Assess for Plasmodium parasites.
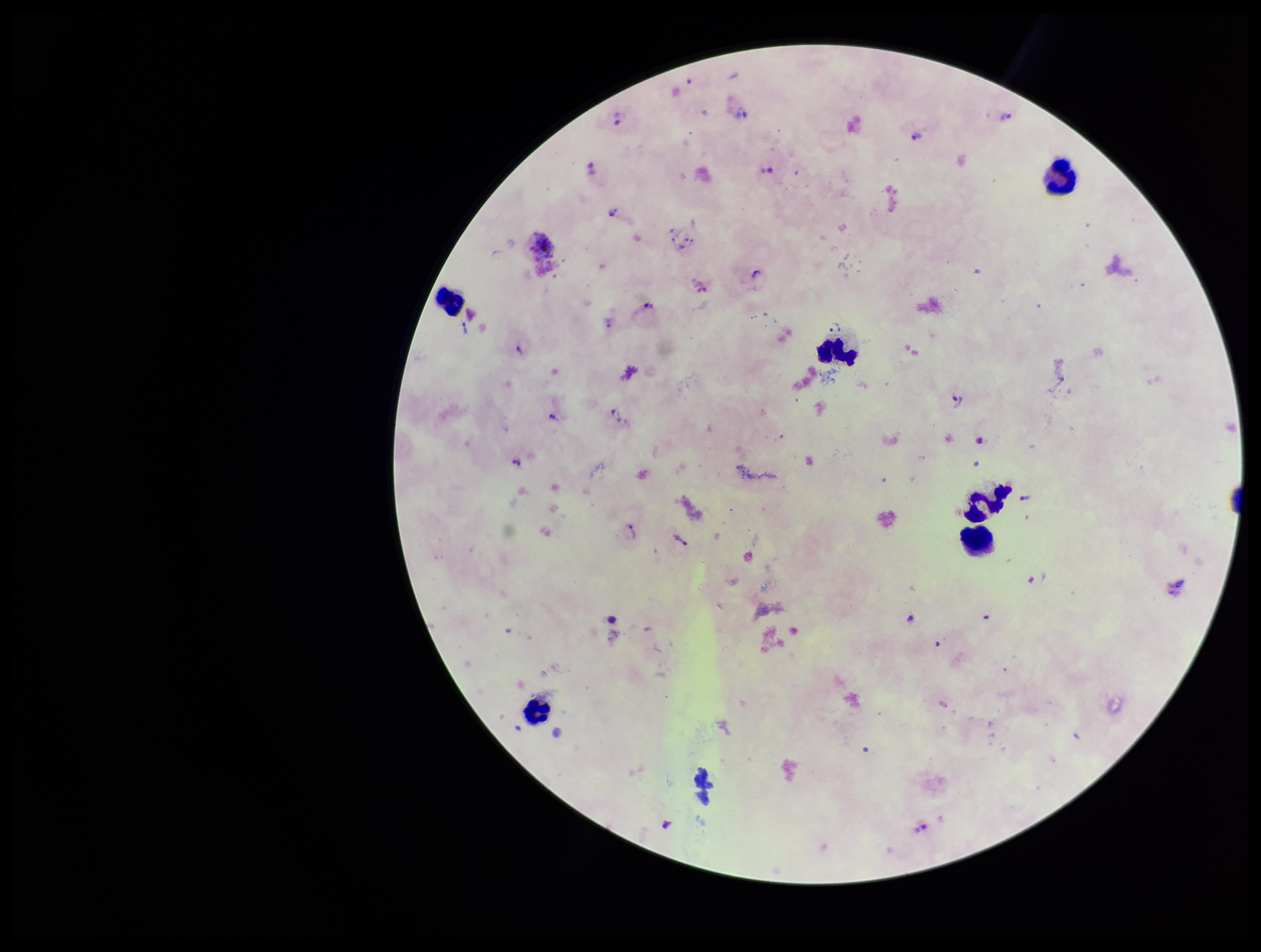

Detected.

Summary:
  - Parasite count: 24
  - Leukocyte count: 6
  - Field of view: single
  - Capture: smartphone photograph through the microscope eyepiece
  - Species reported for this patient: Plasmodium vivax
  - Stain: Giemsa
  - Image size: 1261×952 pixels
  - Preparation: thick smear
  - Patient malaria status: positive